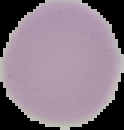

Summary:
  - Image size: 124×130 pixels
  - Malaria status: uninfected
  - Preparation: thin blood smear
  - Image type: cell region segmented out of the field of view; surrounding area masked to black